Identify the parasite.
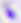
This is Toxoplasma gondii.

modality: photomicrograph
magnification: 400x